Point out each Plasmodium parasite.
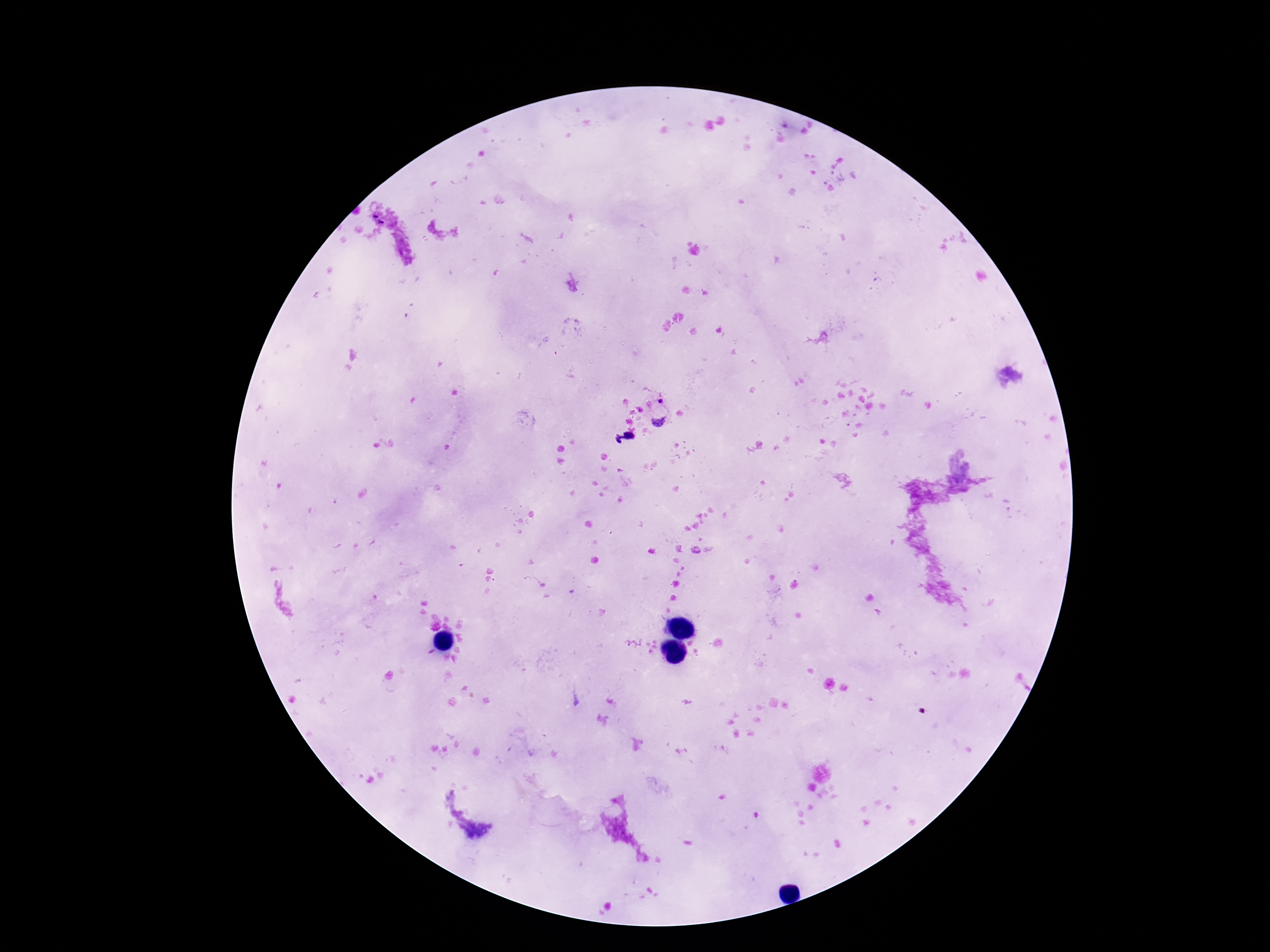

Approximate centers as [x, y] in pixels.
Plasmodium parasites: [659, 410], [624, 438].

magnification = 100x
field of view = single
stain = Giemsa
capture = smartphone camera through the microscope eyepiece
preparation = thick blood film
patient malaria status = infected
image size = 1270×952 pixels